Name the blood parasite species.
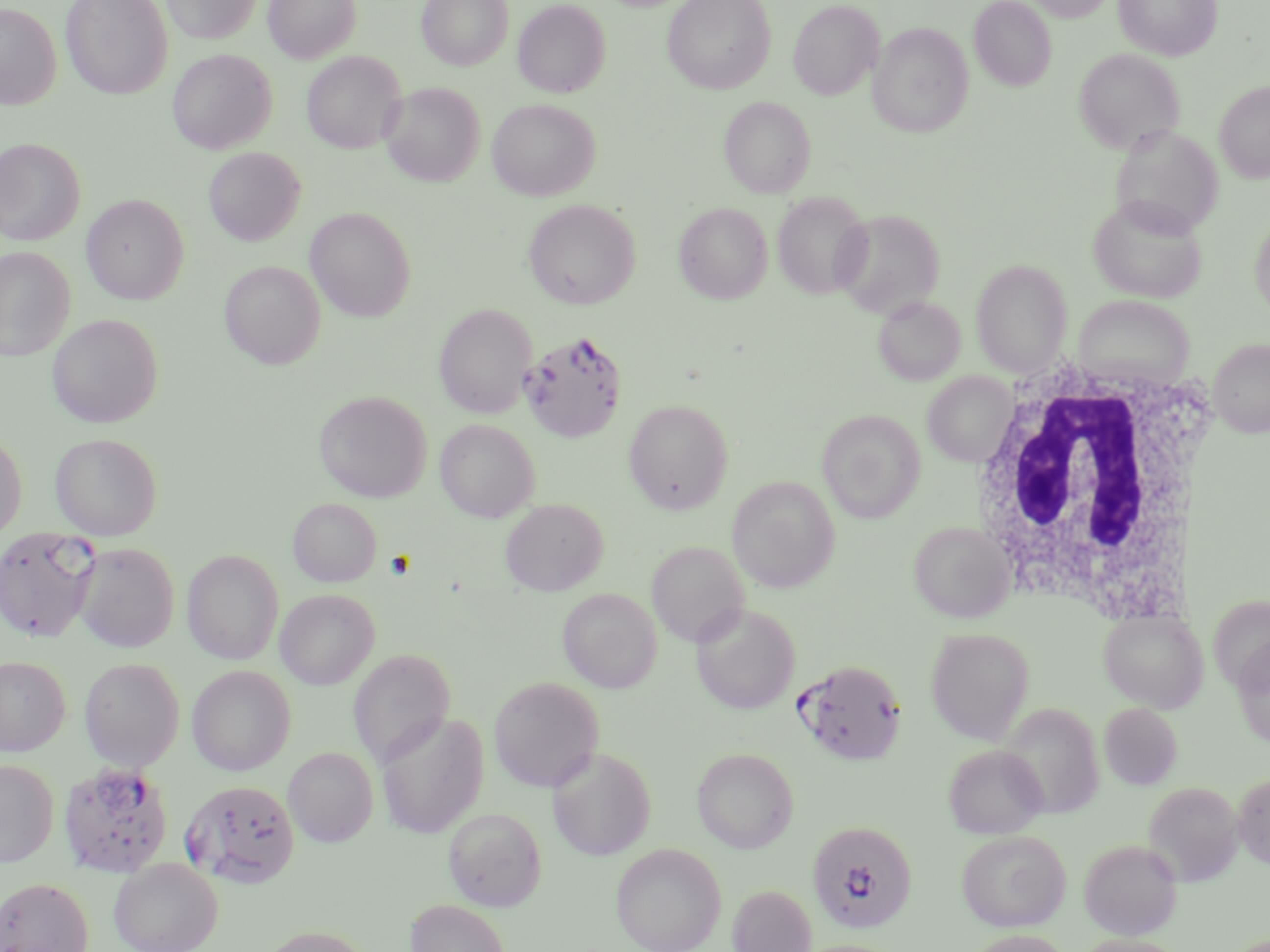
Plasmodium falciparum.

Approximate bounding boxes as (x1,y1)-(x2,y2) corner pairs in pixels. White blood cell locations: (960,356)-(1221,619). Plasmodium falciparum-infected red blood cell locations: (518,329)-(628,443), (0,527)-(101,643), (795,658)-(907,766), (57,761)-(173,879), (182,779)-(300,887), (807,821)-(917,933). Uninfected red blood cell locations: (61,0)-(173,100), (163,0)-(262,44), (264,0)-(361,63), (417,0)-(513,70), (663,0)-(776,94), (969,0)-(1056,91), (1024,0)-(1117,22), (1114,0)-(1222,61), (513,1)-(610,98), (788,1)-(883,99), (0,3)-(62,110), (868,22)-(972,138), (1074,48)-(1185,154), (168,49)-(276,154), (302,51)-(406,154), (1215,81)-(1270,183), (380,82)-(485,186), (719,96)-(815,198), (487,99)-(600,200), (1110,124)-(1224,238), (0,138)-(85,245), (203,147)-(306,245), (772,192)-(872,299), (82,194)-(189,304), (1088,196)-(1207,302), (523,199)-(640,309), (674,202)-(773,304), (305,207)-(417,322), (832,208)-(945,318), (1250,213)-(1270,319), (0,246)-(76,361), (971,259)-(1072,377), (219,260)-(326,369), (873,296)-(965,385), (1075,296)-(1194,389), (434,303)-(537,418), (47,314)-(163,427), (1209,338)-(1270,437), (923,372)-(1015,466), (314,390)-(432,502), (624,399)-(734,515), (817,409)-(925,523), (435,419)-(539,522), (0,430)-(27,543), (50,433)-(163,540), (727,476)-(840,592), (289,498)-(381,587), (500,499)-(608,595), (909,521)-(1015,623), (646,541)-(749,647), (73,543)-(179,653), (182,549)-(284,664), (557,588)-(662,693), (275,589)-(380,690), (691,604)-(800,714), (1099,609)-(1208,713), (926,628)-(1034,744), (1232,639)-(1270,748), (349,648)-(455,766), (0,655)-(69,756), (79,658)-(185,771), (187,665)-(296,775), (489,675)-(604,792), (1100,703)-(1182,789), (1000,704)-(1104,819), (375,711)-(489,839), (943,744)-(1047,839), (547,746)-(656,860), (283,747)-(378,846), (692,747)-(798,853), (0,759)-(59,867), (1232,771)-(1270,870), (1143,781)-(1244,885), (443,806)-(547,911), (956,830)-(1070,931), (1079,839)-(1182,940), (610,843)-(726,952), (109,858)-(222,952), (0,877)-(93,952), (727,884)-(816,952), (405,899)-(510,952), (258,925)-(376,952), (964,930)-(1073,952), (1068,935)-(1192,952), (792,939)-(905,952). Thin blood film. Optical microscopy. Image is 1270×952 pixels. May-Grünwald-Giemsa stain. Captured at 1000x magnification. One field of a larger specimen.